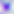 400x magnification. Toxoplasma gondii is shown. Micrograph.